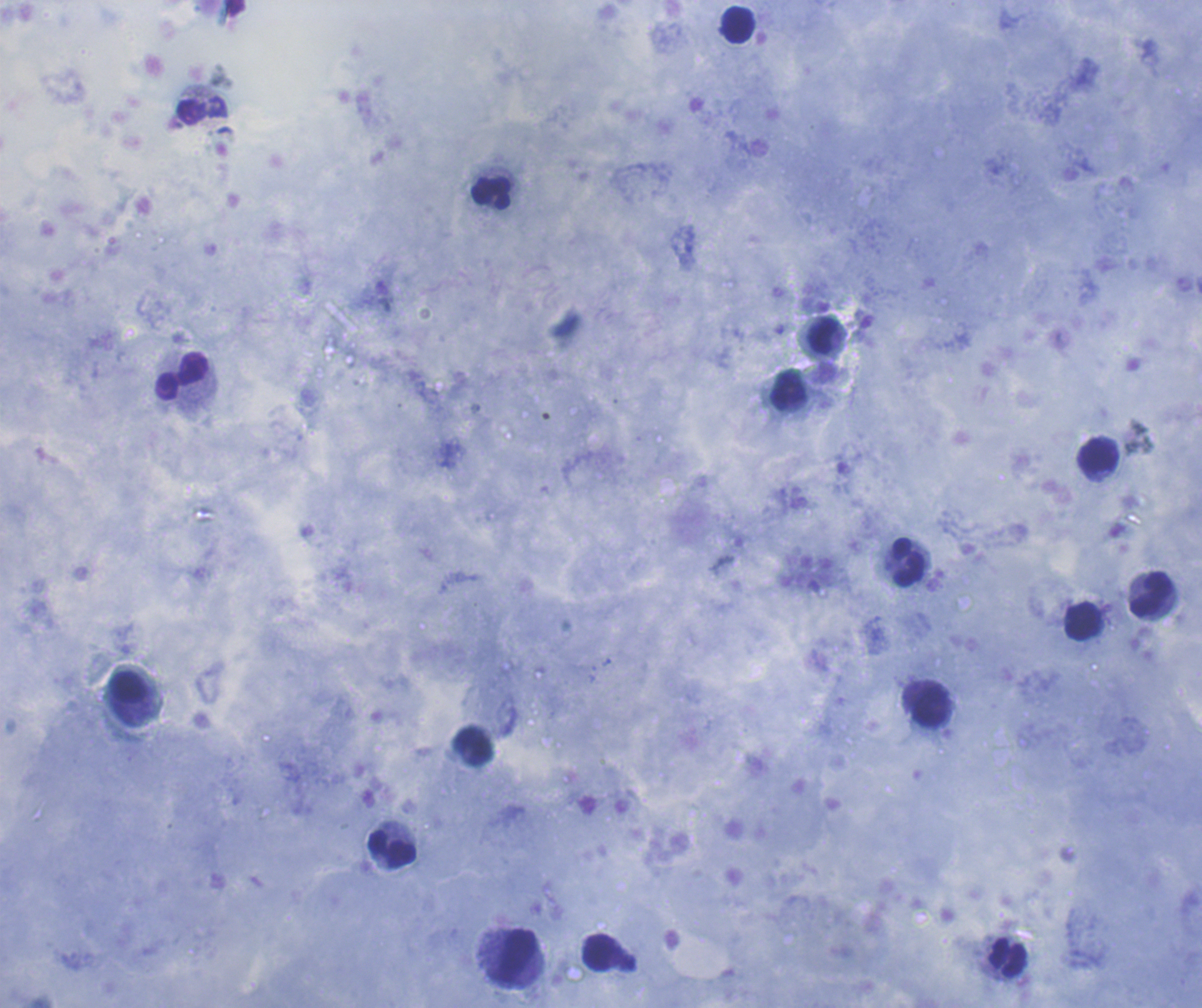
Approximate centers as (x, y) in pixels.
Summary:
  - Leukocyte locations: (737, 25), (203, 111), (492, 193), (822, 336), (180, 375), (788, 390), (1099, 457), (906, 562), (1151, 596), (1082, 621), (129, 688), (931, 706), (391, 850), (598, 952), (514, 957), (1007, 957)
  - Background quality: good
  - Stain: Romanowsky
  - Magnification: 100x
  - Coloration quality: good
  - Context: previously used in a real diagnosis
  - Image size: 1202×1008 pixels
  - Result: negative for malaria parasites
  - Preparation: thick smear of blood
  - Field of view: one from this slide